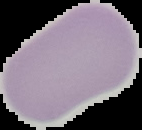 Malaria status: uninfected. Image is 142×130 pixels. Segmented cell region on a black background. From a thin blood smear.